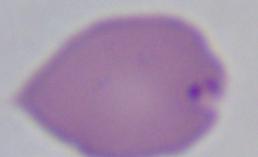

Photomicrograph. A Babesia parasite is shown. 1000x magnification.